Outline each blood parasite and name the species.
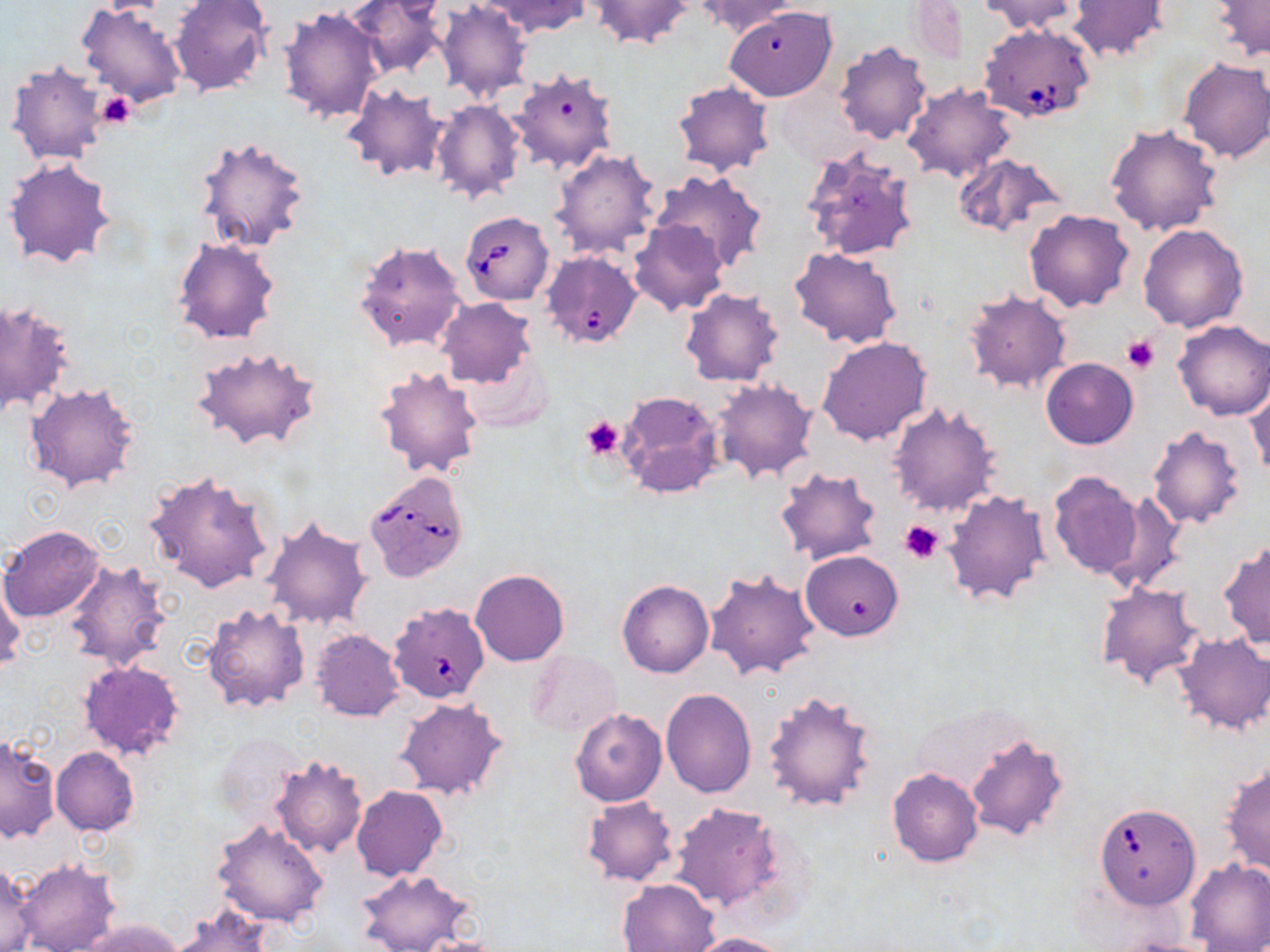
Approximate bounding boxes as named x1/y1/x2/y2 corners in pixels.
Babesia divergens-infected red blood cells: (x1=979, y1=22, x2=1097, y2=123), (x1=459, y1=211, x2=554, y2=304), (x1=542, y1=252, x2=642, y2=348), (x1=365, y1=471, x2=470, y2=582), (x1=388, y1=602, x2=492, y2=703), (x1=1095, y1=807, x2=1201, y2=916).
No Plasmodium falciparum, Plasmodium ovale, Plasmodium malariae, Plasmodium vivax, or Trypanosoma brucei observed.

slide-level diagnosis = Babesia divergens
image size = 1270×952 pixels
stain = May-Grünwald-Giemsa
field of view = single
preparation = thin blood film
platelet locations = approximate bounding boxes as named x1/y1/x2/y2 corners in pixels: (x1=95, y1=92, x2=135, y2=129), (x1=1121, y1=334, x2=1159, y2=373), (x1=582, y1=417, x2=625, y2=460), (x1=897, y1=518, x2=946, y2=564)
modality = light microscopy
magnification = 1000x
uninfected red blood cell locations = approximate bounding boxes as named x1/y1/x2/y2 corners in pixels: (x1=344, y1=0, x2=450, y2=78), (x1=483, y1=0, x2=589, y2=37), (x1=589, y1=0, x2=696, y2=49), (x1=694, y1=0, x2=803, y2=37), (x1=906, y1=0, x2=967, y2=64), (x1=977, y1=0, x2=1082, y2=35), (x1=1211, y1=0, x2=1270, y2=62), (x1=169, y1=1, x2=272, y2=96), (x1=436, y1=2, x2=533, y2=102), (x1=1067, y1=2, x2=1169, y2=61), (x1=77, y1=3, x2=189, y2=109), (x1=278, y1=5, x2=385, y2=125), (x1=728, y1=8, x2=836, y2=100), (x1=834, y1=42, x2=931, y2=144), (x1=1178, y1=57, x2=1270, y2=163), (x1=5, y1=59, x2=110, y2=166), (x1=508, y1=68, x2=619, y2=176), (x1=673, y1=81, x2=774, y2=177), (x1=903, y1=83, x2=1018, y2=184), (x1=342, y1=84, x2=448, y2=182), (x1=432, y1=99, x2=527, y2=204), (x1=1104, y1=122, x2=1225, y2=237), (x1=193, y1=136, x2=311, y2=257), (x1=799, y1=146, x2=920, y2=263), (x1=550, y1=148, x2=662, y2=259), (x1=952, y1=153, x2=1068, y2=238), (x1=4, y1=157, x2=116, y2=270), (x1=645, y1=168, x2=769, y2=273), (x1=1024, y1=209, x2=1136, y2=312), (x1=628, y1=218, x2=728, y2=316), (x1=1139, y1=223, x2=1249, y2=331), (x1=171, y1=235, x2=282, y2=345), (x1=354, y1=239, x2=468, y2=353), (x1=789, y1=247, x2=903, y2=349), (x1=681, y1=288, x2=784, y2=387), (x1=961, y1=288, x2=1072, y2=395), (x1=1, y1=297, x2=75, y2=418), (x1=435, y1=298, x2=536, y2=389), (x1=1172, y1=319, x2=1270, y2=421), (x1=817, y1=334, x2=932, y2=445), (x1=191, y1=346, x2=322, y2=452), (x1=1041, y1=357, x2=1138, y2=448), (x1=374, y1=364, x2=484, y2=479), (x1=712, y1=377, x2=818, y2=484), (x1=1245, y1=379, x2=1269, y2=482), (x1=26, y1=382, x2=140, y2=492), (x1=617, y1=389, x2=723, y2=498), (x1=886, y1=402, x2=1003, y2=518), (x1=1147, y1=426, x2=1247, y2=529), (x1=773, y1=465, x2=883, y2=567), (x1=1047, y1=469, x2=1144, y2=581), (x1=143, y1=470, x2=277, y2=594), (x1=942, y1=488, x2=1052, y2=608), (x1=1105, y1=490, x2=1187, y2=594), (x1=261, y1=518, x2=372, y2=631), (x1=1, y1=525, x2=105, y2=622), (x1=1219, y1=539, x2=1269, y2=651), (x1=800, y1=550, x2=903, y2=640), (x1=63, y1=558, x2=172, y2=670), (x1=0, y1=567, x2=25, y2=674), (x1=705, y1=568, x2=820, y2=682), (x1=470, y1=569, x2=570, y2=666), (x1=1094, y1=580, x2=1207, y2=688), (x1=617, y1=581, x2=713, y2=678), (x1=202, y1=602, x2=310, y2=714), (x1=311, y1=628, x2=404, y2=721), (x1=1173, y1=632, x2=1270, y2=736), (x1=527, y1=648, x2=623, y2=738), (x1=77, y1=658, x2=186, y2=763), (x1=661, y1=689, x2=755, y2=796), (x1=763, y1=689, x2=878, y2=814), (x1=394, y1=698, x2=508, y2=801), (x1=570, y1=709, x2=666, y2=807), (x1=212, y1=733, x2=304, y2=822), (x1=1, y1=735, x2=59, y2=843), (x1=964, y1=735, x2=1069, y2=841), (x1=51, y1=747, x2=140, y2=836), (x1=271, y1=753, x2=368, y2=858), (x1=1220, y1=759, x2=1270, y2=878), (x1=886, y1=768, x2=984, y2=867), (x1=351, y1=785, x2=448, y2=882), (x1=582, y1=796, x2=677, y2=885), (x1=669, y1=802, x2=788, y2=915), (x1=212, y1=820, x2=330, y2=928), (x1=1186, y1=857, x2=1270, y2=951), (x1=13, y1=858, x2=121, y2=952), (x1=0, y1=863, x2=36, y2=952), (x1=357, y1=870, x2=476, y2=952), (x1=617, y1=878, x2=719, y2=951), (x1=170, y1=904, x2=273, y2=952), (x1=80, y1=918, x2=184, y2=952), (x1=686, y1=932, x2=792, y2=952), (x1=1111, y1=934, x2=1225, y2=952)